Locate every parasitized red blood cell.
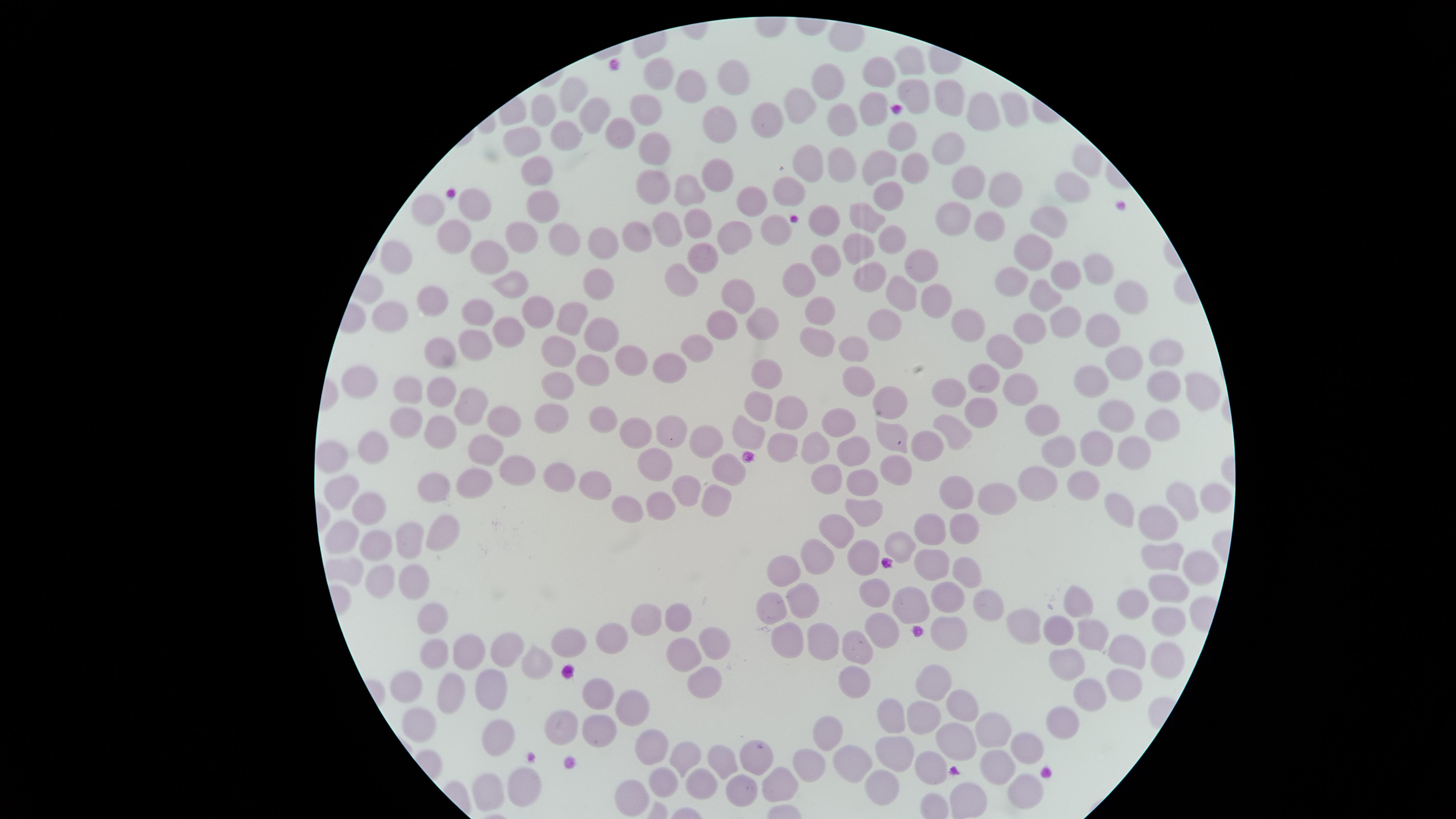

No parasitized red blood cells identified.

image_size: 1456×819 pixels
uninfected_red_blood_cells: 'approximate marker points as {x, y} in pixels: {910, 68}, {733, 73}, {660, 75}, {879, 77}, {826, 83}, {697, 87}, {915, 91}, {576, 92}, {947, 99}, {544, 106}, {795, 109}, {1017, 109}, {646, 112}, {597, 113}, {873, 116}, {767, 120}, {838, 120}, {986, 121}, {720, 124}, {618, 131}, {562, 135}, {901, 137}, {525, 138}, {651, 147}, {947, 148}, {1086, 160}, {809, 162}, {845, 165}, {880, 166}, {538, 168}, {914, 173}, {713, 177}, {653, 186}, {966, 186}, {998, 186}, {1075, 187}, {690, 191}, {788, 191}, {888, 197}, {474, 202}, {539, 202}, {755, 202}, {432, 205}, {868, 218}, {957, 219}, {989, 219}, {701, 223}, {1056, 223}, {775, 224}, {826, 226}, {454, 230}, {668, 230}, {525, 235}, {634, 235}, {563, 238}, {734, 240}, {893, 240}, {595, 247}, {861, 250}, {1031, 250}, {488, 255}, {701, 256}, {394, 258}, {826, 261}, {1094, 262}, {923, 267}, {1065, 275}, {683, 277}, {801, 280}, {1010, 280}, {508, 282}, {869, 282}, {595, 287}, {736, 291}, {901, 295}, {1126, 295}, {1037, 296}, {929, 298}, {435, 301}, {537, 306}, {471, 308}, {819, 310}, {388, 314}, {962, 319}, {570, 321}, {757, 321}, {1061, 323}, {720, 326}, {889, 327}, {1104, 329}, {508, 330}, {1026, 331}, {598, 335}, {815, 345}, {699, 348}, {853, 348}, {1001, 348}, {474, 349}, {552, 349}, {436, 355}, {1170, 355}, {630, 356}, {1128, 364}, {662, 367}, {592, 370}, {765, 372}, {979, 376}, {1092, 378}, {359, 380}, {857, 383}, {558, 387}, {1014, 387}, {1159, 387}, {1197, 387}, {407, 391}, {438, 394}, {890, 397}, {951, 397}, {474, 404}, {976, 407}, {759, 408}, {787, 412}, {1115, 416}, {549, 418}, {601, 419}, {833, 419}, {1161, 419}, {507, 422}, {1040, 423}, {401, 428}, {952, 429}, {664, 430}, {890, 432}, {437, 433}, {637, 433}, {748, 440}, {706, 441}, {482, 444}, {819, 444}, {783, 446}, {932, 446}, {1093, 448}, {1135, 449}, {857, 450}, {379, 451}, {1063, 453}, {327, 455}, {651, 463}, {517, 467}, {725, 470}, {896, 476}, {561, 477}, {822, 479}, {1044, 479}, {479, 482}, {863, 483}, {594, 484}, {437, 486}, {689, 486}, {1088, 486}, {341, 489}, {954, 492}, {1179, 495}, {1215, 498}, {1007, 499}, {659, 507}, {370, 509}, {624, 509}, {711, 509}, {1125, 509}, {864, 513}, {1167, 522}, {838, 526}, {962, 528}, {440, 531}, {930, 531}, {342, 532}, {412, 541}, {897, 546}, {374, 547}, {1159, 551}, {867, 558}, {816, 559}, {933, 563}, {1198, 570}, {785, 572}, {963, 572}, {414, 575}, {376, 576}, {1169, 589}, {800, 593}, {874, 595}, {947, 598}, {1082, 603}, {915, 605}, {1137, 605}, {986, 606}, {771, 609}, {679, 610}, {433, 612}, {641, 619}, {1170, 622}, {877, 625}, {1028, 627}, {1063, 631}, {939, 633}, {784, 636}, {822, 639}, {1095, 639}, {614, 640}, {714, 642}, {570, 644}, {511, 647}, {435, 648}, {473, 648}, {858, 648}, {1170, 649}, {686, 652}, {1129, 654}, {1071, 661}, {539, 663}, {702, 680}, {855, 683}, {926, 683}, {1128, 683}, {407, 691}, {451, 691}, {1086, 695}, {596, 698}, {496, 699}, {961, 701}, {638, 713}, {919, 714}, {889, 718}, {418, 723}, {1061, 723}, {563, 731}, {993, 732}, {594, 733}, {823, 735}, {956, 740}, {505, 744}, {1030, 747}, {655, 748}, {896, 753}, {683, 757}, {756, 759}, {855, 760}, {716, 762}, {933, 767}, {997, 767}, {808, 769}, {693, 781}, {776, 782}, {659, 783}, {524, 785}, {882, 788}, {489, 789}, {737, 790}, {1026, 792}, {634, 797}'
capture: smartphone photograph through the microscope eyepiece
field_of_view: single
visible_region: circular
preparation: thin blood smear
stain: Giemsa